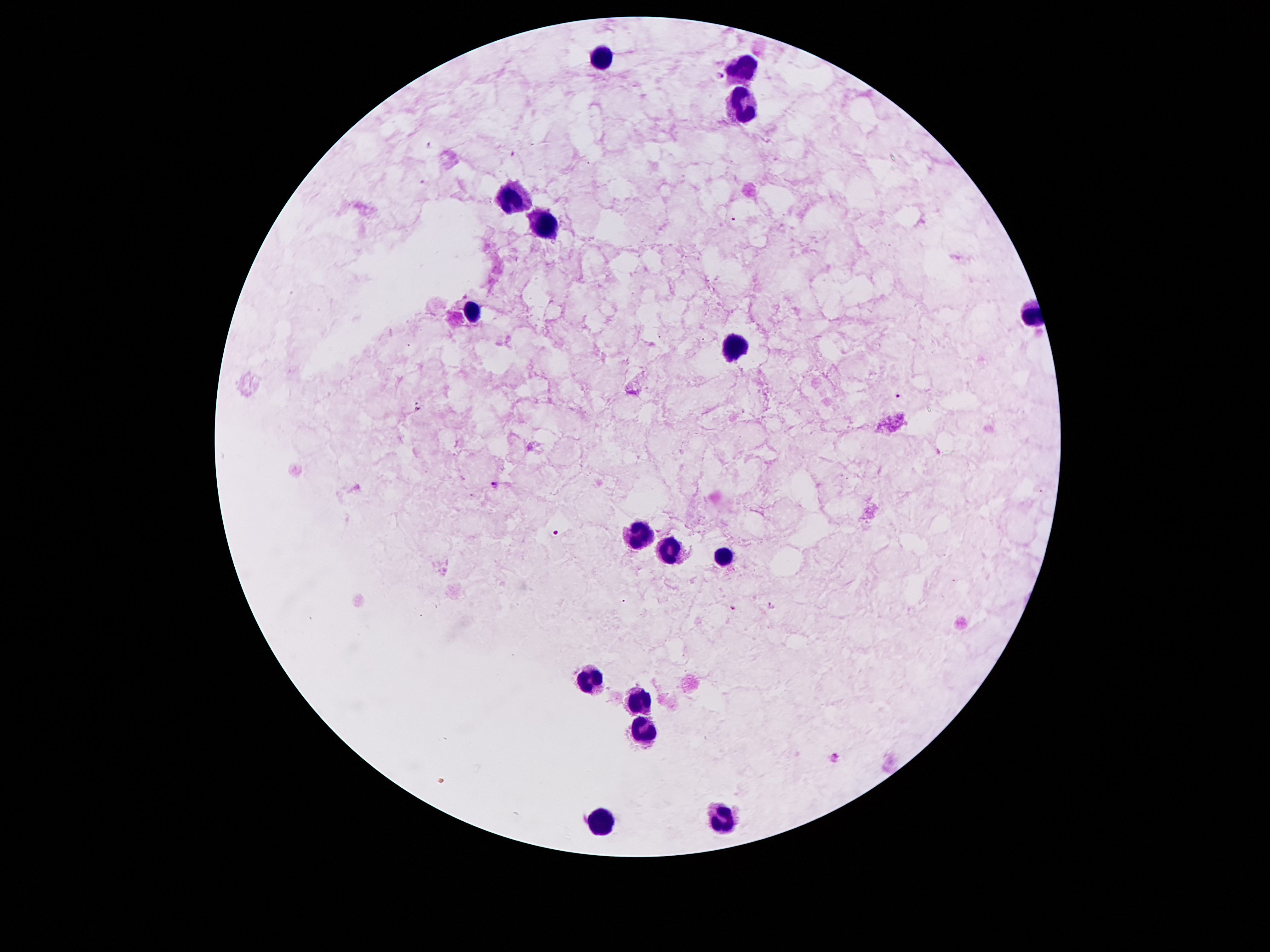

Approximate centers as (x, y) in pixels. Leukocyte locations: (745, 59), (603, 60), (739, 106), (509, 197), (539, 223), (471, 313), (729, 340), (629, 535), (669, 554), (721, 554), (593, 679), (637, 702), (645, 731), (718, 820), (599, 825). Plasmodium parasite locations: (719, 77), (899, 395), (495, 485), (557, 532), (769, 605), (735, 609), (834, 758). Giemsa-stained preparation. 100x magnification. Image is 1270×952 pixels. Patient malaria status: infected with Plasmodium falciparum. Thick blood smear. Photographed through the microscope eyepiece with a smartphone camera. One field from this slide.